State the blood parasite species.
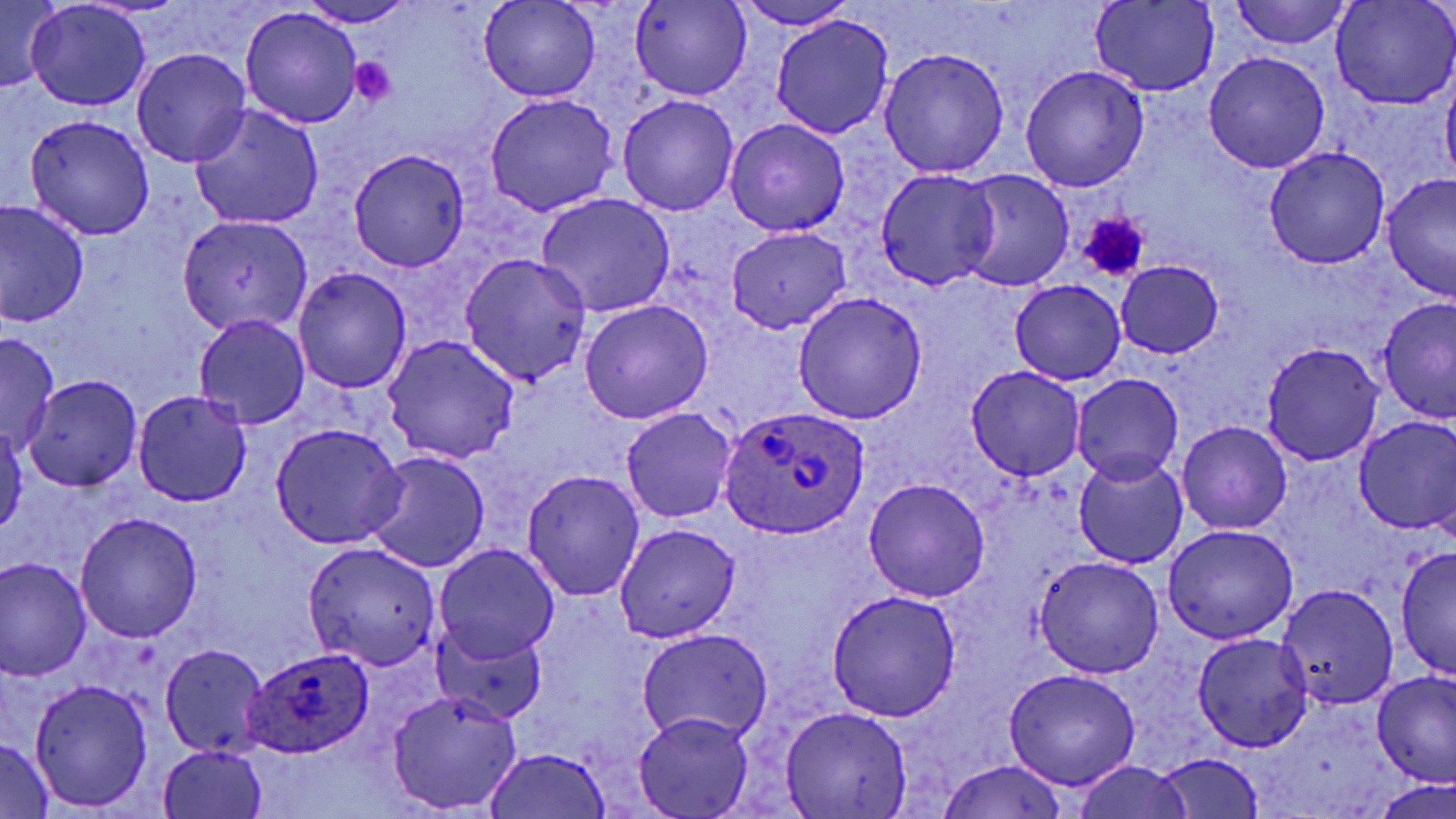
Plasmodium ovale.

uninfected red blood cell locations = approximate bounding boxes as (x1,y1)-(x2,y2) corner pairs in pixels: (0,0)-(62,94), (631,0)-(751,101), (732,0)-(861,29), (1331,0)-(1455,108), (295,1)-(420,27), (479,1)-(599,103), (1230,1)-(1351,50), (25,2)-(149,111), (1089,2)-(1219,96), (240,9)-(361,128), (771,15)-(894,141), (879,46)-(1009,177), (132,49)-(251,167), (1204,51)-(1330,173), (1019,65)-(1150,191), (1441,74)-(1456,190), (483,94)-(619,217), (618,94)-(739,215), (191,104)-(324,229), (24,115)-(156,240), (725,119)-(850,235), (1264,146)-(1390,269), (349,150)-(469,272), (876,169)-(1000,290), (955,171)-(1075,292), (1381,175)-(1455,303), (536,193)-(675,317), (0,200)-(90,325), (179,216)-(312,335), (728,227)-(850,334), (458,253)-(591,386), (1116,261)-(1224,358), (292,267)-(412,394), (1009,280)-(1126,384), (792,291)-(927,425), (1378,298)-(1456,423), (579,300)-(713,424), (194,315)-(310,430), (0,332)-(60,453), (383,335)-(518,464), (1261,342)-(1383,466), (967,365)-(1087,481), (1072,373)-(1183,486), (24,376)-(142,491), (132,389)-(252,507), (621,407)-(737,523), (1354,415)-(1456,536), (0,420)-(25,540), (1177,421)-(1293,535), (269,422)-(408,549), (363,451)-(490,574), (1072,455)-(1189,570), (521,469)-(645,601), (863,477)-(992,602), (73,513)-(203,642), (615,523)-(740,642), (1161,524)-(1298,645), (302,541)-(441,669), (435,544)-(560,664), (1395,545)-(1455,682), (1034,557)-(1164,678), (0,558)-(92,681), (1277,584)-(1398,709), (827,590)-(961,721), (434,625)-(546,726), (636,628)-(775,746), (1192,633)-(1314,752), (160,643)-(269,759), (1003,668)-(1139,789), (1370,671)-(1456,789), (30,680)-(152,811), (387,689)-(524,814), (781,706)-(913,817), (633,714)-(753,819), (0,740)-(54,818), (158,744)-(269,819), (482,747)-(614,818), (1152,752)-(1266,818), (936,759)-(1071,819), (1069,761)-(1195,819), (1374,779)-(1456,818)
platelet locations = approximate bounding boxes as (x1,y1)-(x2,y2) corner pairs in pixels: (350,57)-(397,106), (1077,213)-(1150,282)
preparation = thin blood film
magnification = 1000x
stain = May-Grünwald-Giemsa
field of view = one of a larger specimen
Plasmodium ovale-infected red blood cell locations = approximate bounding boxes as (x1,y1)-(x2,y2) corner pairs in pixels: (716,405)-(872,537), (231,653)-(373,758)
image size = 1456×819 pixels
modality = optical microscopy